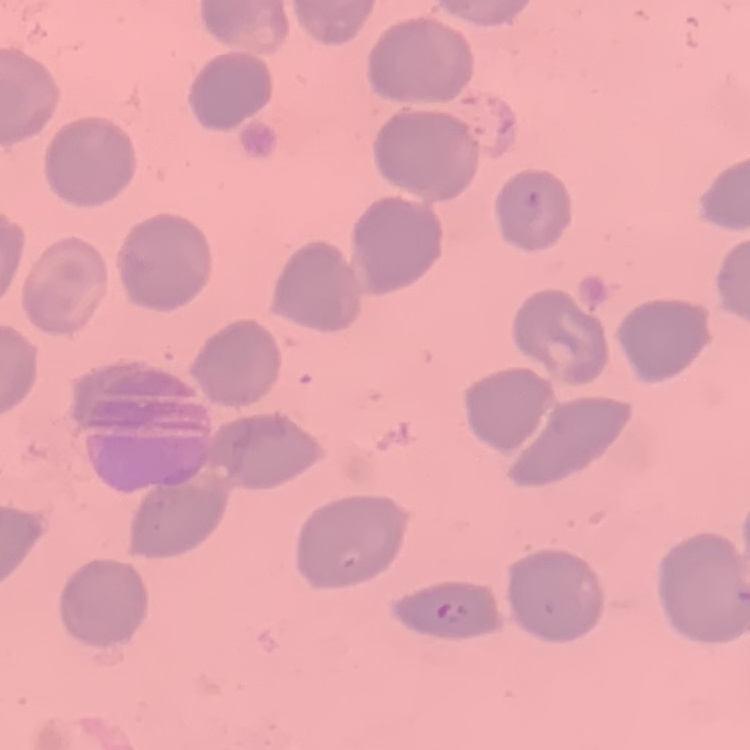 The erythrocytes show no rouleaux formation. Thin blood film. Stained with either Field's or Giemsa. One tile cut from a larger photomicrograph.